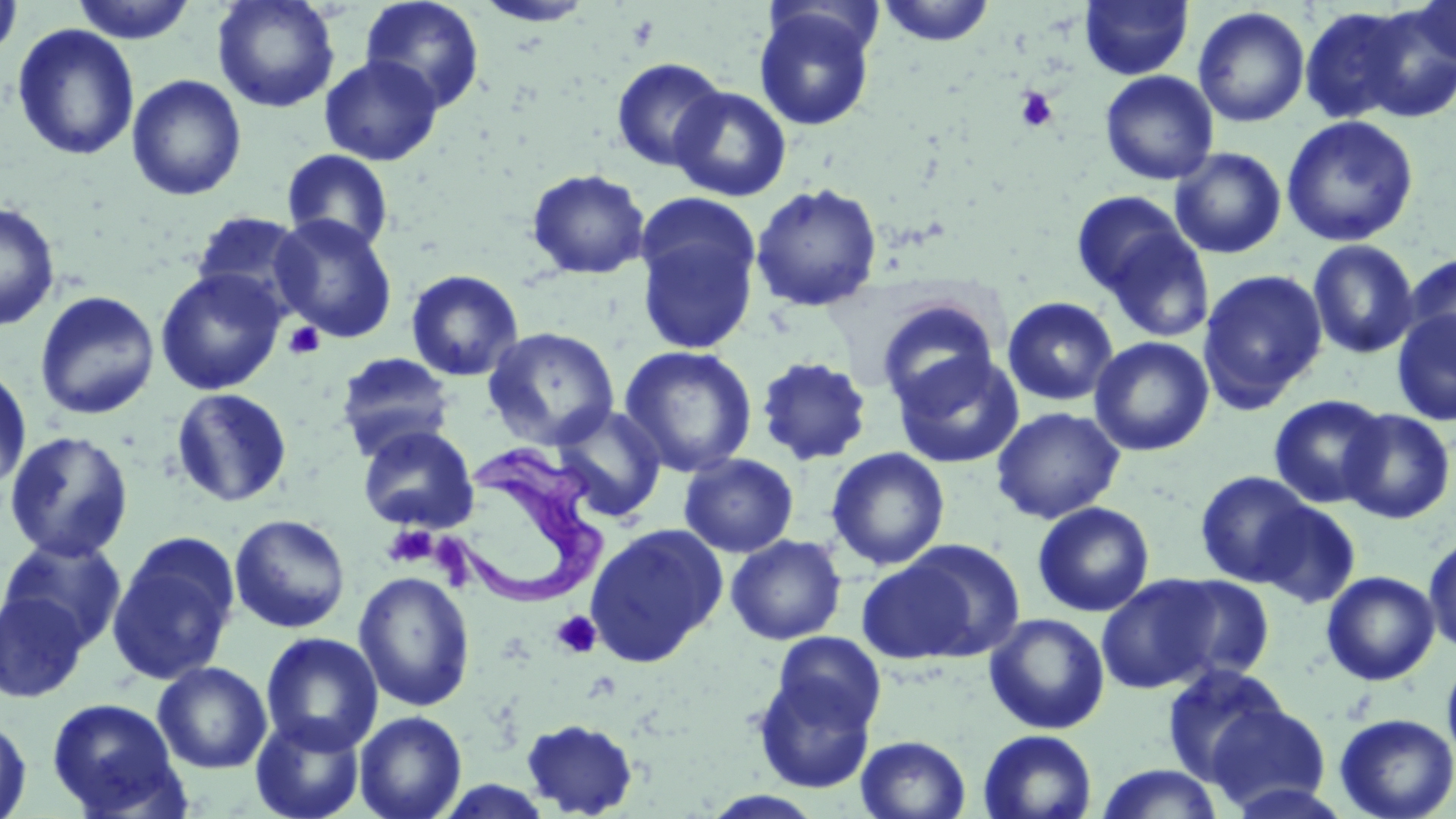

slide-level diagnosis = Trypanosoma brucei
stain = May-Grünwald-Giemsa
preparation = thin blood film
platelet locations = approximate bounding boxes as (x1, y1, x2, y2) in pixels: (1014, 87, 1059, 132), (283, 321, 325, 360), (382, 523, 438, 569), (551, 611, 602, 659)
magnification = 1000x
field of view = one of a larger specimen
Trypanosoma brucei locations = approximate bounding boxes as (x1, y1, x2, y2) in pixels: (442, 444, 614, 612)
image size = 1456×819 pixels
uninfected red blood cell locations = approximate bounding boxes as (x1, y1, x2, y2) in pixels: (0, 0, 24, 61), (69, 0, 199, 45), (212, 0, 340, 113), (359, 0, 485, 113), (877, 0, 996, 47), (1079, 0, 1194, 80), (1411, 0, 1456, 69), (473, 1, 596, 27), (753, 5, 877, 131), (1357, 5, 1456, 120), (1192, 6, 1310, 128), (1298, 6, 1415, 124), (12, 24, 140, 161), (319, 55, 443, 166), (610, 57, 728, 172), (1099, 70, 1219, 185), (126, 74, 247, 201), (669, 85, 792, 202), (1281, 114, 1419, 247), (1170, 148, 1287, 259), (281, 149, 395, 253), (526, 168, 651, 279), (750, 183, 883, 312), (1070, 191, 1193, 301), (0, 201, 61, 331), (634, 202, 761, 356), (189, 210, 313, 317), (271, 215, 398, 344), (1097, 224, 1217, 344), (1307, 239, 1421, 360), (1402, 252, 1456, 356), (154, 268, 287, 395), (405, 269, 524, 381), (1197, 269, 1328, 411), (34, 290, 160, 420), (1002, 296, 1119, 407), (876, 297, 1000, 410), (1391, 308, 1456, 426), (482, 326, 620, 449), (1089, 336, 1214, 456), (618, 345, 758, 478), (891, 351, 1025, 469), (336, 352, 456, 459), (755, 356, 873, 466), (0, 364, 32, 495), (170, 388, 293, 507), (1268, 394, 1389, 509), (552, 405, 667, 523), (991, 406, 1125, 524), (1339, 408, 1456, 524), (357, 424, 479, 533), (3, 431, 135, 563), (826, 447, 950, 570), (679, 453, 799, 558), (1195, 470, 1315, 586), (1254, 499, 1362, 609), (1032, 501, 1155, 617), (229, 513, 350, 633), (584, 523, 728, 667), (1423, 531, 1456, 655), (106, 533, 241, 686), (726, 534, 847, 645), (0, 535, 128, 653), (856, 551, 998, 667), (353, 570, 475, 712), (1321, 570, 1440, 685), (1096, 574, 1234, 693), (1155, 574, 1277, 685), (0, 589, 90, 704), (984, 613, 1110, 735), (771, 631, 886, 735), (260, 632, 383, 755), (1441, 650, 1456, 770), (153, 661, 272, 774), (1160, 662, 1291, 785), (752, 672, 876, 794), (45, 697, 188, 818), (1204, 700, 1333, 815), (354, 710, 467, 819), (250, 713, 367, 819), (1334, 713, 1456, 819), (0, 714, 33, 819), (521, 718, 639, 817), (978, 729, 1097, 819), (855, 734, 971, 819), (1094, 764, 1225, 819), (700, 790, 827, 818)
modality = light microscopy